State which parasite is depicted.
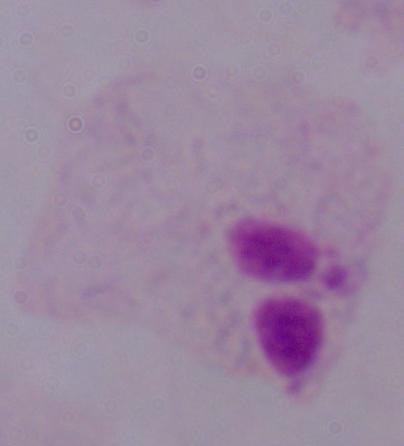
A trichomonad.

modality = photomicrograph
magnification = 1000x